Identify the parasite.
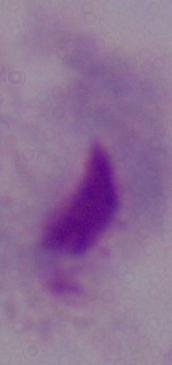
This is a trichomonad.

modality = micrograph
magnification = 1000x